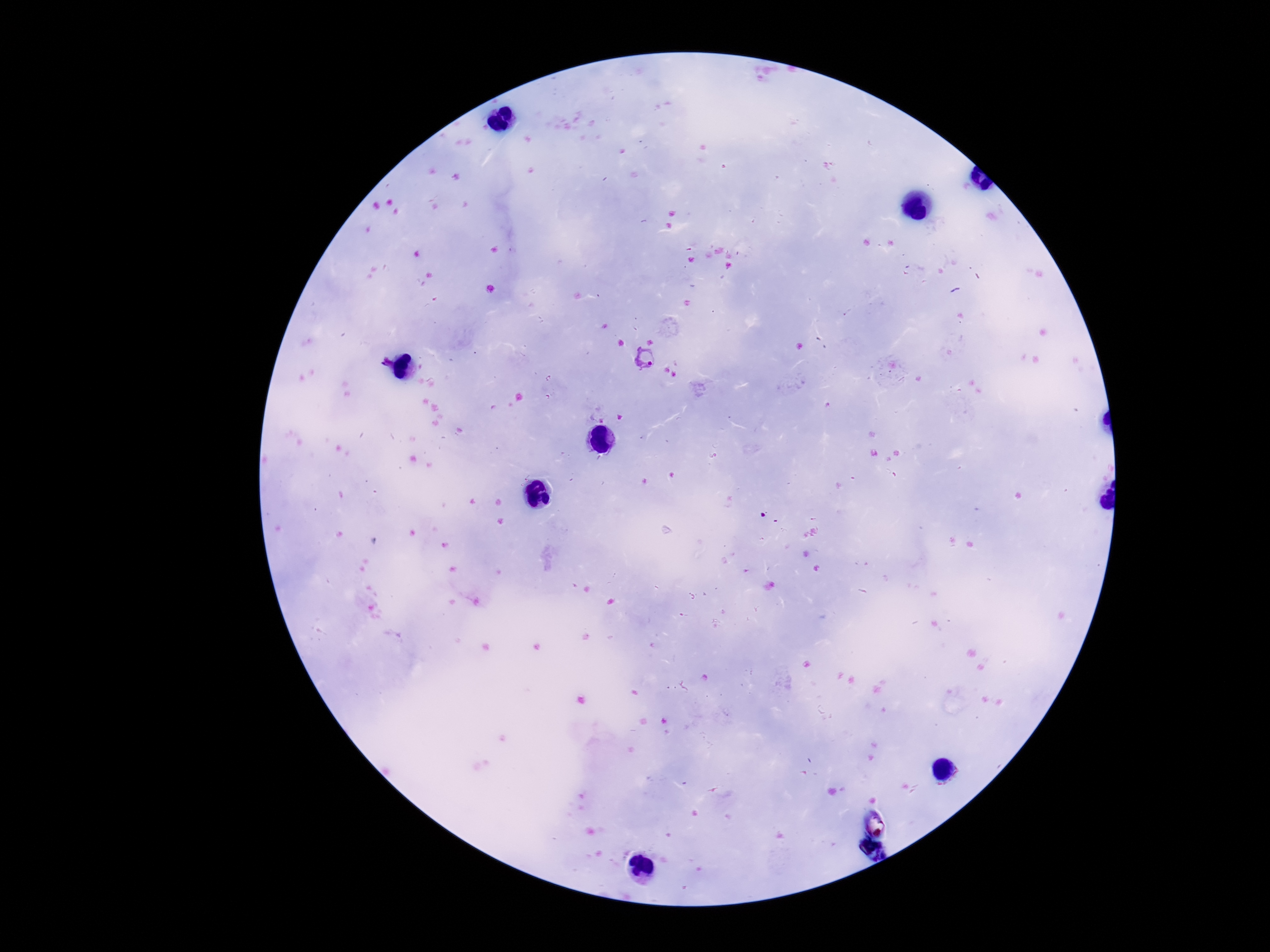

Approximate object centers, in pixels from the top-left corner.
Summary:
  - Plasmodium parasite locations: (x=644, y=359), (x=386, y=363)
  - Image size: 1270×952 pixels
  - Capture: smartphone camera through the microscope eyepiece
  - Patient malaria status: positive
  - Preparation: thick blood smear
  - Magnification: 100x
  - Stain: Giemsa
  - Field of view: one from this slide